Name the parasite shown.
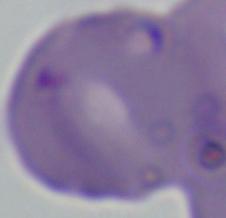

This is Babesia.

Summary:
  - Magnification: 1000x
  - Modality: photomicrograph